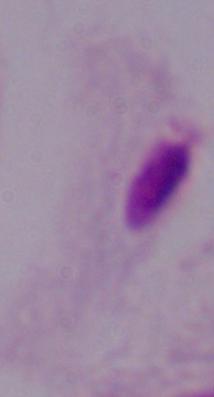

A trichomonad is shown. Photomicrograph. Captured at 1000x magnification.